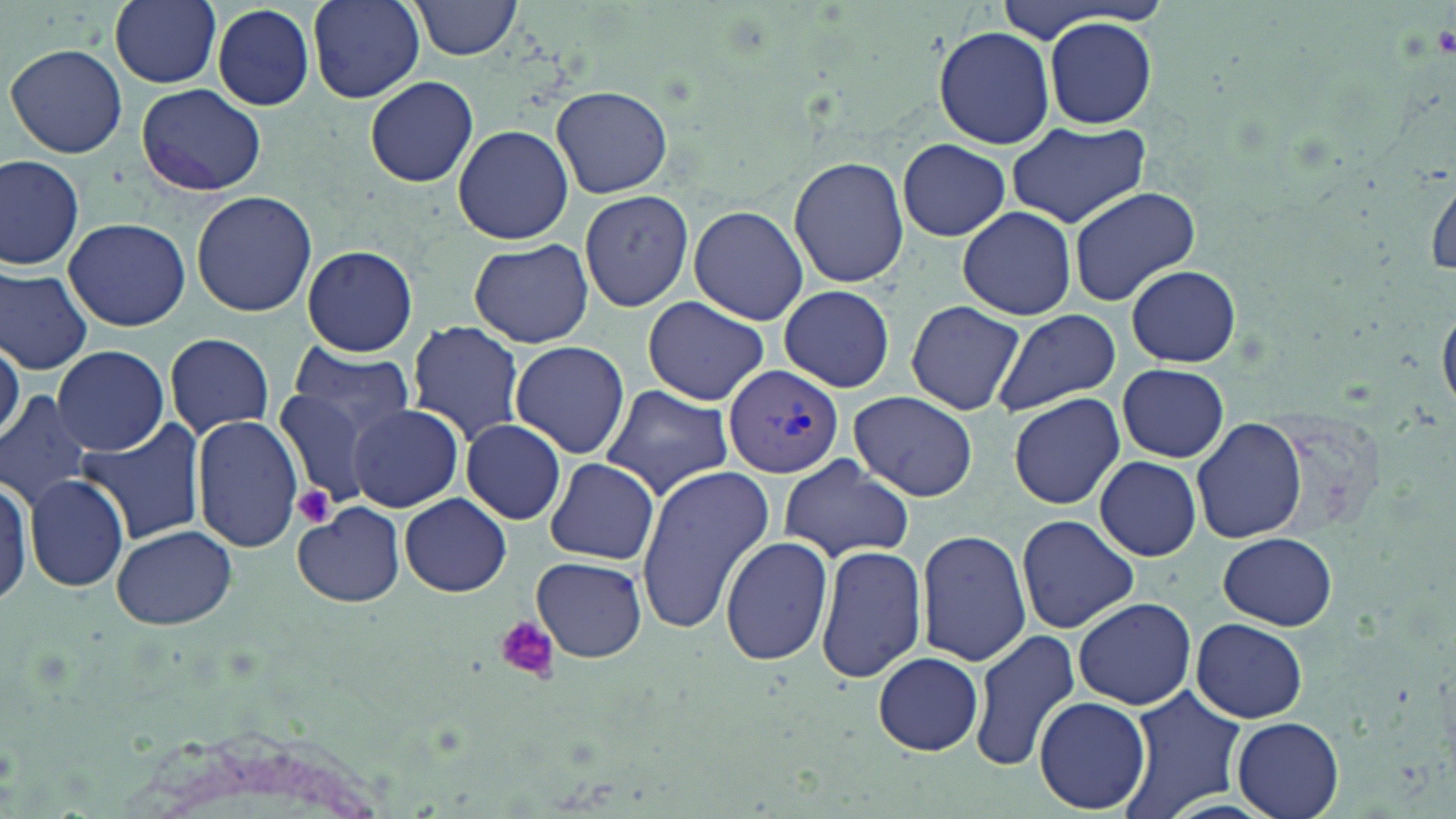

Summary:
  - Coordinate format: approximate bounding boxes as named x1/y1/x2/y2 corners in pixels
  - Plasmodium vivax-infected red blood cell locations: (x1=723, y1=364, x2=845, y2=479)
  - Uninfected red blood cell locations: (x1=110, y1=0, x2=222, y2=88), (x1=306, y1=0, x2=425, y2=103), (x1=411, y1=0, x2=523, y2=60), (x1=208, y1=3, x2=317, y2=111), (x1=1041, y1=14, x2=1159, y2=129), (x1=932, y1=26, x2=1056, y2=149), (x1=6, y1=43, x2=128, y2=159), (x1=365, y1=73, x2=479, y2=188), (x1=137, y1=83, x2=266, y2=197), (x1=552, y1=85, x2=672, y2=199), (x1=1007, y1=121, x2=1149, y2=228), (x1=452, y1=125, x2=573, y2=245), (x1=897, y1=138, x2=1010, y2=241), (x1=0, y1=154, x2=86, y2=271), (x1=789, y1=155, x2=910, y2=288), (x1=1425, y1=164, x2=1456, y2=284), (x1=1068, y1=186, x2=1203, y2=309), (x1=191, y1=190, x2=317, y2=319), (x1=580, y1=190, x2=694, y2=313), (x1=688, y1=205, x2=808, y2=324), (x1=955, y1=206, x2=1077, y2=319), (x1=63, y1=216, x2=191, y2=331), (x1=469, y1=238, x2=593, y2=348), (x1=298, y1=246, x2=420, y2=357), (x1=1125, y1=264, x2=1241, y2=367), (x1=0, y1=268, x2=92, y2=374), (x1=774, y1=287, x2=895, y2=392), (x1=640, y1=296, x2=769, y2=405), (x1=905, y1=300, x2=1026, y2=416), (x1=991, y1=307, x2=1121, y2=416), (x1=406, y1=322, x2=524, y2=444), (x1=165, y1=331, x2=275, y2=438), (x1=0, y1=336, x2=23, y2=443), (x1=509, y1=340, x2=630, y2=460), (x1=53, y1=344, x2=169, y2=457), (x1=285, y1=345, x2=415, y2=437), (x1=1117, y1=364, x2=1230, y2=462), (x1=599, y1=384, x2=735, y2=501), (x1=272, y1=387, x2=385, y2=503), (x1=0, y1=389, x2=97, y2=512), (x1=845, y1=391, x2=979, y2=501), (x1=1007, y1=392, x2=1126, y2=510), (x1=347, y1=404, x2=464, y2=512), (x1=192, y1=414, x2=302, y2=554), (x1=72, y1=418, x2=204, y2=546), (x1=1190, y1=418, x2=1307, y2=545), (x1=462, y1=419, x2=566, y2=525), (x1=460, y1=437, x2=646, y2=540), (x1=775, y1=453, x2=913, y2=563), (x1=1094, y1=455, x2=1201, y2=561), (x1=543, y1=459, x2=661, y2=566), (x1=632, y1=463, x2=775, y2=635), (x1=24, y1=473, x2=130, y2=591), (x1=400, y1=493, x2=512, y2=597), (x1=293, y1=502, x2=406, y2=608), (x1=1016, y1=514, x2=1138, y2=634), (x1=111, y1=525, x2=239, y2=632), (x1=915, y1=529, x2=1030, y2=666), (x1=1218, y1=532, x2=1336, y2=630), (x1=720, y1=536, x2=833, y2=666), (x1=816, y1=542, x2=928, y2=685), (x1=530, y1=556, x2=647, y2=664), (x1=1073, y1=597, x2=1196, y2=711), (x1=1191, y1=619, x2=1308, y2=723), (x1=967, y1=628, x2=1083, y2=772), (x1=874, y1=653, x2=983, y2=755), (x1=1117, y1=686, x2=1245, y2=819), (x1=1036, y1=695, x2=1150, y2=815), (x1=1231, y1=716, x2=1345, y2=819)
  - Platelet locations: (x1=291, y1=483, x2=337, y2=529), (x1=494, y1=616, x2=558, y2=682)
  - Slide-level diagnosis: Plasmodium vivax
  - Field of view: one of a larger specimen
  - Stain: May-Grünwald-Giemsa
  - Preparation: thin blood film
  - Magnification: 1000x
  - Modality: optical microscopy
  - Image size: 1456×819 pixels